Identify the blood parasite species.
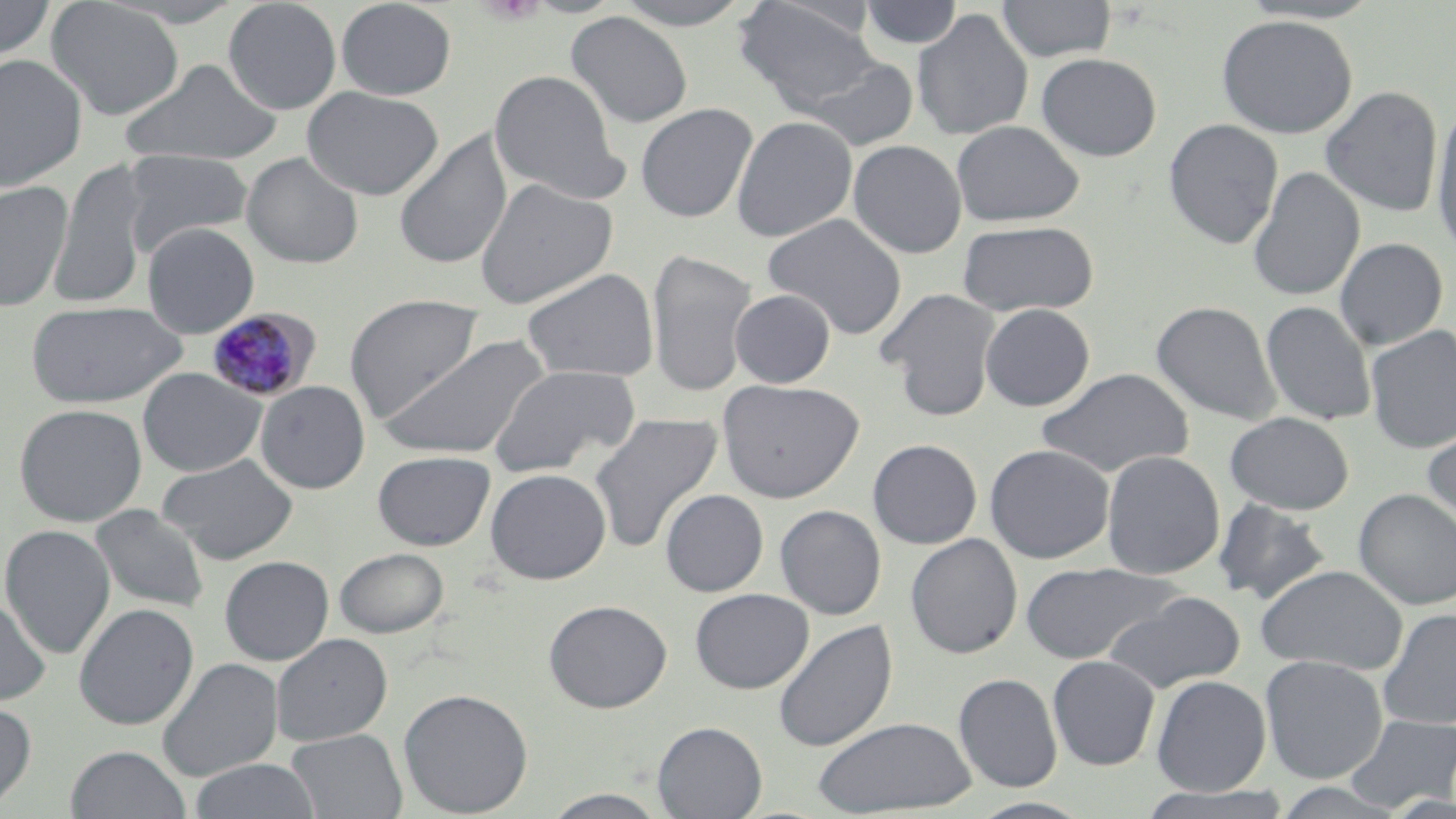

Plasmodium malariae.

{
  "preparation": "thin blood film",
  "modality": "optical microscopy",
  "field_of_view": "single",
  "plasmodium_malariae_infected_red_blood_cell_locations": "approximate bounding boxes as (x1, y1, x2, y2) in pixels: (206, 307, 320, 403)",
  "platelet_locations": "approximate bounding boxes as (x1, y1, x2, y2) in pixels: (475, 0, 547, 25)",
  "stain": "May-Grünwald-Giemsa",
  "image_size": "1456×819 pixels",
  "uninfected_red_blood_cell_locations": "approximate bounding boxes as (x1, y1, x2, y2) in pixels: (0, 0, 57, 63), (46, 0, 184, 120), (222, 0, 342, 114), (335, 0, 457, 100), (611, 0, 758, 29), (996, 0, 1117, 62), (1237, 0, 1385, 24), (733, 1, 882, 113), (859, 1, 964, 49), (912, 9, 1034, 142), (565, 11, 694, 128), (1217, 14, 1357, 138), (1036, 51, 1163, 162), (0, 53, 88, 193), (799, 55, 919, 152), (119, 58, 285, 167), (489, 70, 625, 201), (1320, 85, 1443, 217), (301, 86, 445, 200), (635, 103, 758, 223), (1430, 103, 1456, 262), (731, 115, 858, 242), (1163, 118, 1284, 250), (951, 120, 1084, 227), (393, 131, 513, 269), (848, 139, 967, 259), (122, 149, 253, 255), (241, 152, 364, 268), (49, 158, 151, 309), (1247, 166, 1365, 302), (473, 178, 618, 308), (0, 179, 73, 312), (762, 213, 907, 340), (956, 220, 1099, 317), (142, 222, 260, 338), (1334, 237, 1448, 350), (645, 248, 758, 397), (520, 267, 660, 383), (877, 288, 1001, 421), (730, 289, 836, 388), (344, 294, 484, 422), (25, 299, 187, 409), (1151, 300, 1282, 425), (1260, 301, 1377, 427), (980, 303, 1095, 411), (1364, 325, 1456, 455), (382, 333, 551, 460), (488, 363, 641, 476), (138, 367, 266, 477), (1037, 367, 1194, 478), (717, 378, 864, 503), (255, 381, 371, 493), (14, 403, 147, 526), (1225, 411, 1354, 514), (590, 413, 724, 553), (1421, 416, 1456, 531), (867, 439, 982, 549), (984, 443, 1116, 563), (372, 450, 495, 550), (1101, 450, 1225, 580), (157, 454, 299, 564), (485, 468, 612, 585), (660, 488, 768, 596), (1353, 488, 1456, 610), (1213, 498, 1332, 605), (775, 504, 887, 619), (90, 505, 210, 614), (1, 524, 116, 659), (905, 533, 1023, 659), (334, 547, 449, 638), (219, 555, 334, 665), (1019, 562, 1182, 665), (1255, 564, 1409, 675), (690, 588, 814, 693), (1103, 591, 1246, 694), (0, 592, 51, 708), (544, 599, 672, 713), (74, 603, 199, 730), (1377, 608, 1456, 731), (773, 619, 898, 752), (270, 633, 393, 745), (1047, 655, 1160, 771), (1259, 655, 1388, 784), (157, 657, 283, 782), (953, 672, 1062, 792), (1151, 675, 1271, 796), (399, 688, 534, 817), (0, 700, 37, 811), (1342, 713, 1456, 812), (812, 715, 977, 816), (652, 721, 767, 819), (286, 728, 407, 819), (65, 745, 191, 819), (189, 758, 321, 819), (1268, 781, 1411, 818), (1136, 784, 1297, 819), (540, 789, 673, 818), (968, 797, 1096, 819)",
  "magnification": "1000x"
}